Classify this cell by malaria status.
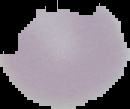
It is uninfected.

Summary:
  - Image type: segmented cell region with the area outside set to black
  - Preparation: thin blood film
  - Image size: 130×109 pixels